Classify this cell by malaria status.
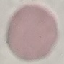

Uninfected.

Summary:
  - Preparation: thin smear
  - Capture: smartphone camera at the microscope eyepiece
  - Image type: automatically extracted cell patch, resized to 64 × 64 pixels
  - Stain: Giemsa